Classify this cell by malaria status.
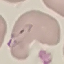

It is parasitized.

Acquired by smartphone through the microscope eyepiece. Giemsa stain. Thin smear of blood. Automatically extracted cell patch, resized to 64 × 64 pixels.